Locate every Plasmodium falciparum-infected red blood cell.
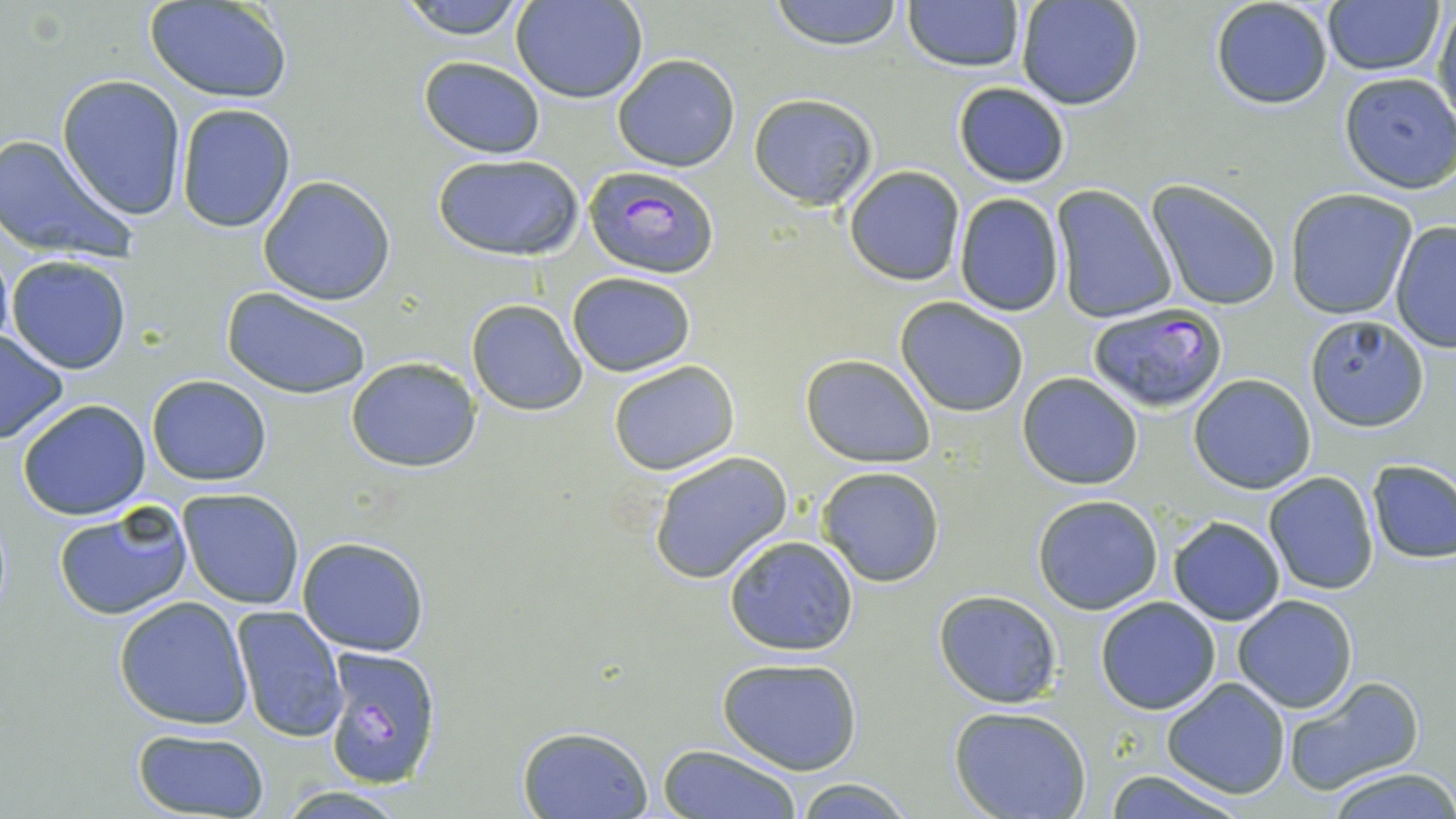

Approximate bounding boxes as (x1,y1)-(x2,y2) corner pairs in pixels.
Plasmodium falciparum-infected red blood cells: (582,166)-(718,278), (1087,303)-(1227,413), (323,647)-(442,790).

Uninfected red blood cell locations: (145,0)-(294,103), (392,0)-(533,39), (511,0)-(647,103), (768,0)-(905,49), (902,0)-(1025,72), (1014,1)-(1144,110), (1209,1)-(1335,111), (1322,1)-(1444,75), (1433,4)-(1456,125), (612,54)-(740,172), (419,55)-(546,158), (1339,72)-(1456,193), (56,75)-(188,220), (952,81)-(1071,187), (748,93)-(878,209), (174,103)-(297,233), (0,131)-(139,262), (433,151)-(586,262), (843,166)-(965,285), (257,175)-(397,305), (1145,181)-(1282,314), (1051,186)-(1178,324), (1285,189)-(1420,321), (953,192)-(1064,316), (1389,219)-(1456,353), (7,255)-(132,374), (566,272)-(695,376), (222,287)-(373,400), (895,297)-(1029,418), (466,299)-(588,416), (1303,314)-(1430,431), (0,329)-(70,444), (800,353)-(935,466), (345,357)-(482,473), (608,360)-(739,475), (1017,372)-(1144,491), (1190,374)-(1316,494), (147,375)-(272,486), (16,400)-(152,519), (646,450)-(793,584), (1366,460)-(1456,565), (816,465)-(945,587), (1263,473)-(1379,594), (178,489)-(306,609), (1031,494)-(1164,614), (52,501)-(194,621), (1168,516)-(1285,625), (723,534)-(861,657), (297,536)-(430,656), (934,591)-(1062,708), (114,595)-(252,730), (1233,595)-(1358,713), (1095,597)-(1221,715), (230,605)-(346,743), (718,656)-(862,775), (1281,676)-(1425,796), (1161,677)-(1290,799), (949,707)-(1093,819), (516,725)-(653,819), (132,729)-(269,817), (657,745)-(801,819), (1324,768)-(1456,819), (1101,770)-(1252,819), (793,778)-(915,817), (272,786)-(415,817). Slide-level diagnosis: Plasmodium falciparum. Image is 1456×819 pixels. One field of a larger specimen. Light microscopy. May-Grünwald-Giemsa-stained preparation. 1000x magnification. Thin blood smear.